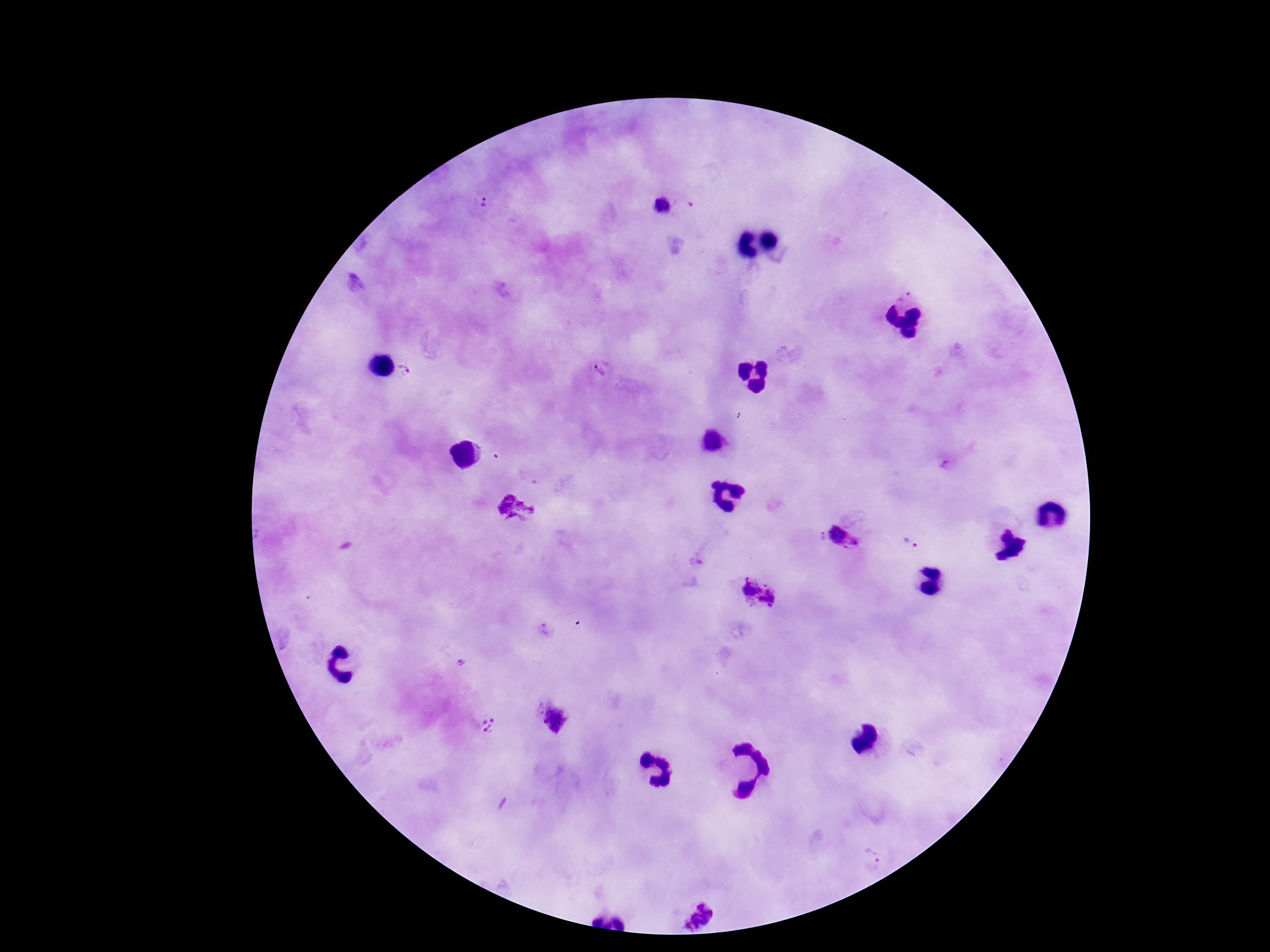

{
  "stain": "Giemsa",
  "capture": "smartphone camera through the microscope eyepiece",
  "preparation": "thick blood smear",
  "plasmodium_parasite_locations": "approximate centers as [x, y] in pixels: [482, 205], [662, 205], [600, 368], [406, 371], [514, 510], [820, 537], [844, 538], [909, 544], [546, 631], [462, 661], [555, 721], [488, 726], [873, 854], [695, 915]",
  "magnification": "100x",
  "patient_malaria_status": "infected",
  "image_size": "1270×952 pixels",
  "field_of_view": "one from this slide"
}